State which parasite is depicted.
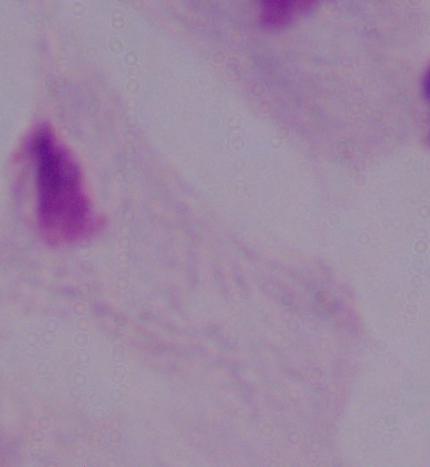

A trichomonad.

Summary:
  - Modality: micrograph
  - Magnification: 1000x